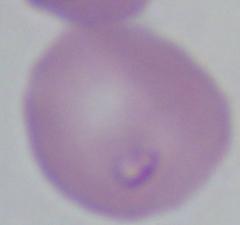

Summary:
  - Magnification: 1000x
  - Identification: Babesia
  - Modality: micrograph